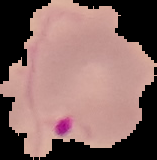
preparation = thin blood smear
image type = segmented cell region on a black background
image size = 157×160 pixels
malaria status = parasitized